Assess this cell for malaria.
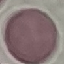

Uninfected.

preparation = thin blood smear
capture = smartphone camera at the microscope eyepiece
stain = Giemsa
image type = cell patch, automatically extracted from a larger field of view and resized to 64 × 64 pixels